Locate every blood parasite and identify its species.
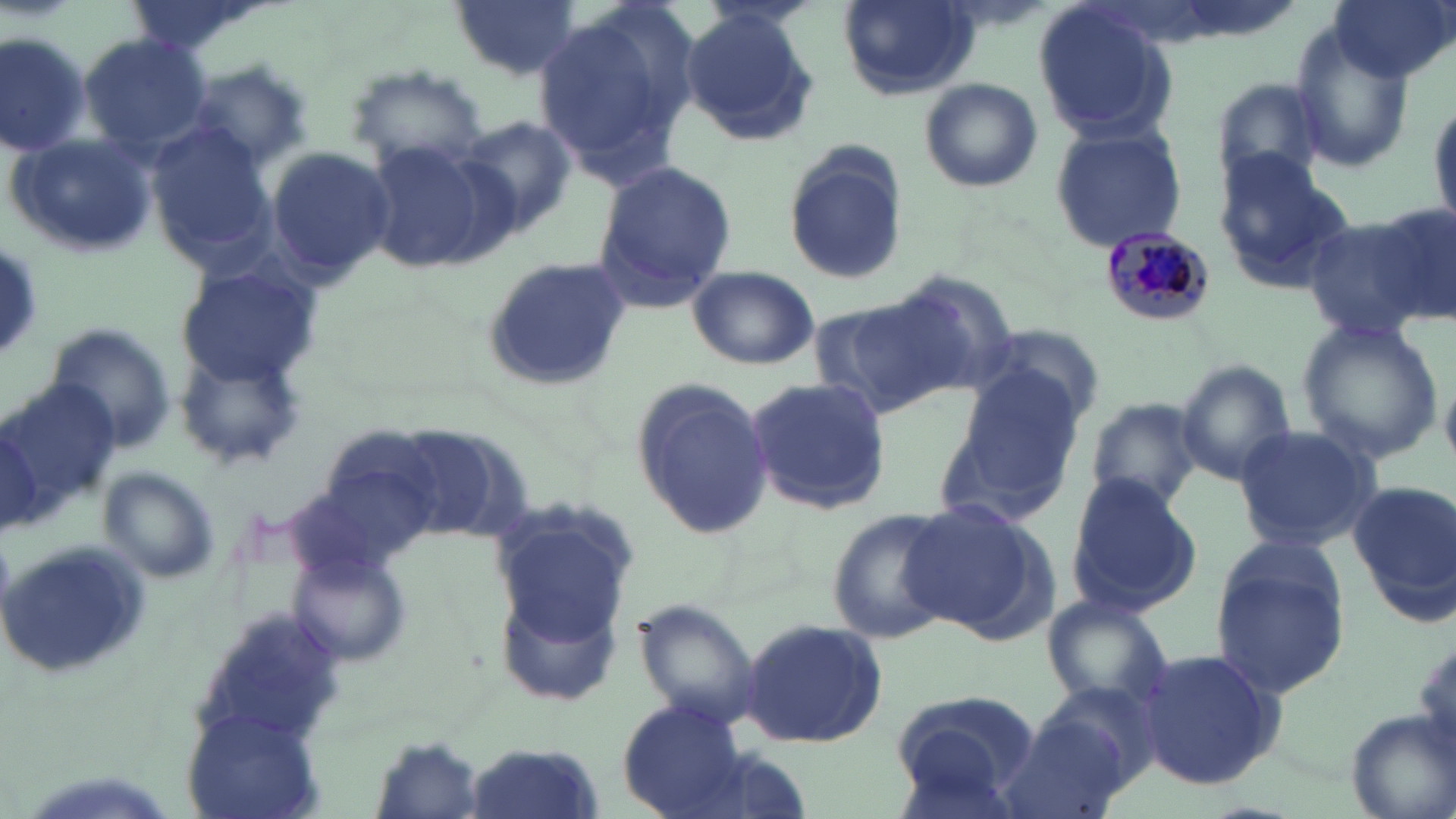
Approximate bounding boxes as named x1/y1/x2/y2 corners in pixels.
Plasmodium malariae-infected red blood cells: (x1=1099, y1=229, x2=1216, y2=329).
No Plasmodium falciparum, Plasmodium ovale, Plasmodium vivax, Babesia divergens, or Trypanosoma brucei observed.

Summary:
  - Uninfected red blood cell locations: (x1=447, y1=0, x2=580, y2=80), (x1=1032, y1=0, x2=1178, y2=144), (x1=1328, y1=0, x2=1454, y2=84), (x1=839, y1=1, x2=976, y2=100), (x1=533, y1=2, x2=698, y2=177), (x1=679, y1=6, x2=819, y2=146), (x1=1290, y1=25, x2=1417, y2=167), (x1=1, y1=29, x2=93, y2=159), (x1=78, y1=33, x2=214, y2=155), (x1=183, y1=62, x2=313, y2=170), (x1=346, y1=66, x2=490, y2=176), (x1=918, y1=76, x2=1043, y2=192), (x1=1209, y1=78, x2=1327, y2=190), (x1=1429, y1=92, x2=1456, y2=232), (x1=455, y1=113, x2=580, y2=240), (x1=1048, y1=121, x2=1190, y2=252), (x1=146, y1=126, x2=281, y2=263), (x1=7, y1=135, x2=158, y2=259), (x1=363, y1=137, x2=506, y2=273), (x1=782, y1=144, x2=909, y2=287), (x1=265, y1=145, x2=395, y2=284), (x1=1211, y1=149, x2=1353, y2=290), (x1=591, y1=157, x2=736, y2=308), (x1=1366, y1=200, x2=1456, y2=325), (x1=1300, y1=216, x2=1438, y2=341), (x1=0, y1=243, x2=47, y2=359), (x1=481, y1=256, x2=631, y2=391), (x1=173, y1=260, x2=319, y2=387), (x1=687, y1=266, x2=819, y2=369), (x1=887, y1=269, x2=1020, y2=396), (x1=809, y1=294, x2=961, y2=419), (x1=1296, y1=318, x2=1444, y2=466), (x1=42, y1=322, x2=179, y2=455), (x1=979, y1=322, x2=1104, y2=427), (x1=175, y1=343, x2=310, y2=469), (x1=1173, y1=360, x2=1296, y2=488), (x1=949, y1=368, x2=1088, y2=508), (x1=745, y1=377, x2=890, y2=513), (x1=627, y1=381, x2=777, y2=541), (x1=4, y1=383, x2=124, y2=512), (x1=1087, y1=398, x2=1203, y2=512), (x1=0, y1=417, x2=46, y2=533), (x1=1231, y1=424, x2=1381, y2=551), (x1=98, y1=468, x2=221, y2=585), (x1=1063, y1=473, x2=1203, y2=615), (x1=1349, y1=480, x2=1455, y2=612), (x1=897, y1=498, x2=1052, y2=640), (x1=488, y1=499, x2=638, y2=649), (x1=828, y1=504, x2=958, y2=642), (x1=1, y1=541, x2=152, y2=682), (x1=1210, y1=544, x2=1351, y2=701), (x1=293, y1=552, x2=414, y2=666), (x1=1040, y1=591, x2=1174, y2=711), (x1=631, y1=597, x2=761, y2=732), (x1=738, y1=618, x2=888, y2=750), (x1=1411, y1=630, x2=1454, y2=756), (x1=1132, y1=646, x2=1287, y2=794), (x1=889, y1=693, x2=1037, y2=813), (x1=617, y1=698, x2=749, y2=819), (x1=1341, y1=709, x2=1455, y2=819), (x1=178, y1=711, x2=327, y2=819), (x1=999, y1=714, x2=1132, y2=819), (x1=366, y1=738, x2=490, y2=819), (x1=465, y1=741, x2=602, y2=819)
  - Slide-level diagnosis: Plasmodium malariae
  - Stain: May-Grünwald-Giemsa
  - Preparation: thin blood smear
  - Image size: 1456×819 pixels
  - Field of view: one of a larger specimen
  - Magnification: 1000x
  - Modality: light microscopy